Give the preparation type.
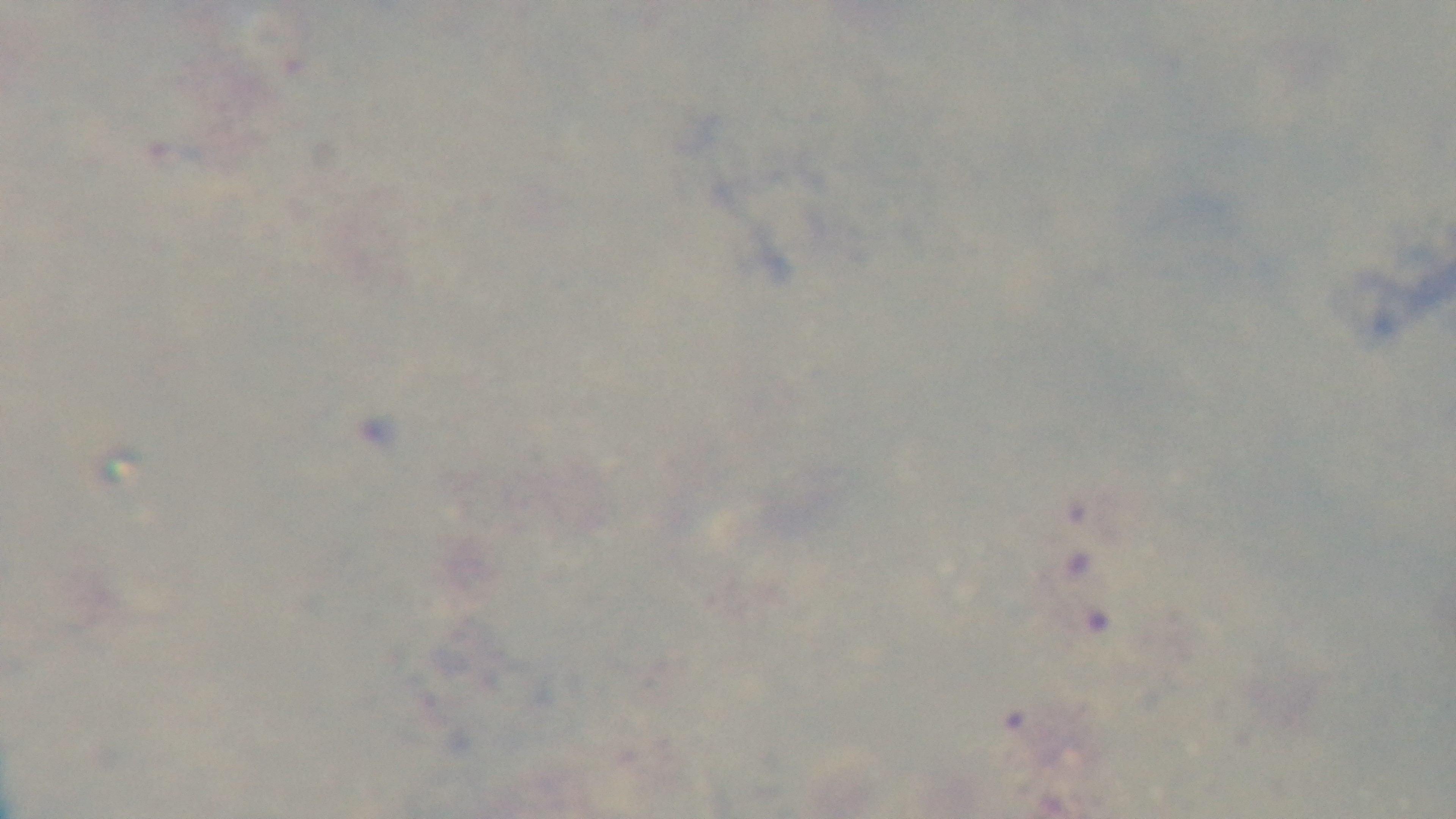

It is a thick blood film.

Photomicrograph. One field from the slide. Oil-immersion objective, 100x. Malaria status: uninfected. Giemsa-stained. Mounted 4K digital camera.